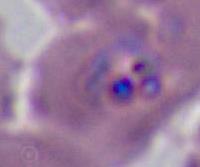

A Plasmodium parasite is shown. Micrograph. 400x or 1000x magnification.